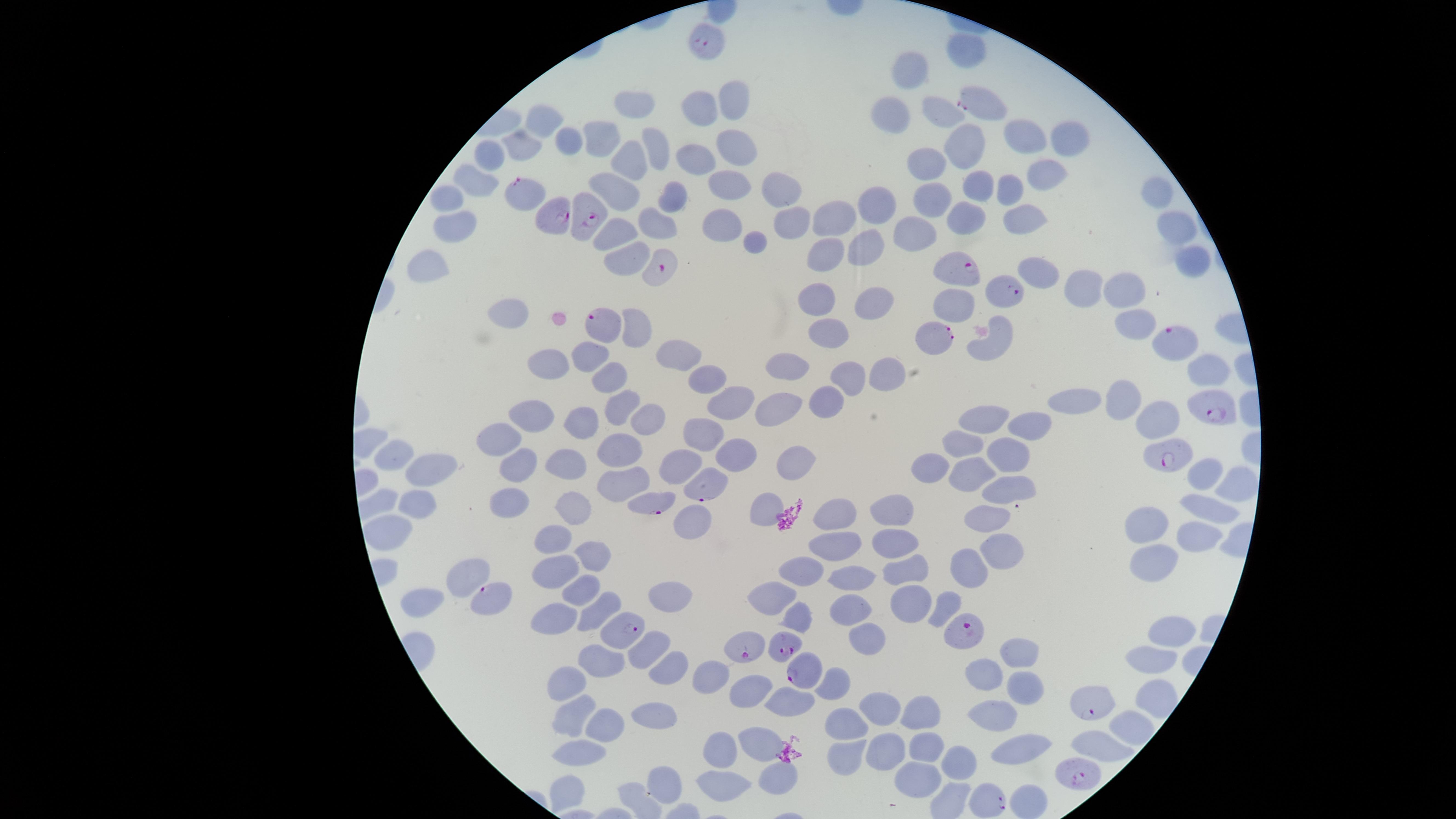
Approximate marker points as {x, y} in pixels. Uninfected RBCs: {966, 45}, {912, 68}, {733, 96}, {635, 103}, {700, 103}, {935, 107}, {894, 112}, {544, 116}, {1023, 134}, {1071, 139}, {608, 140}, {572, 143}, {528, 144}, {657, 145}, {732, 145}, {965, 145}, {491, 155}, {630, 158}, {692, 159}, {927, 165}, {1044, 169}, {728, 179}, {477, 181}, {981, 185}, {1160, 187}, {619, 188}, {780, 188}, {1011, 190}, {935, 193}, {449, 196}, {674, 198}, {877, 203}, {1022, 214}, {964, 216}, {834, 217}, {794, 220}, {723, 224}, {654, 225}, {455, 226}, {914, 227}, {1176, 227}, {617, 229}, {755, 240}, {862, 245}, {825, 253}, {630, 261}, {1189, 262}, {426, 264}, {1037, 270}, {1072, 284}, {1121, 286}, {870, 297}, {820, 298}, {950, 298}, {503, 313}, {1137, 322}, {637, 332}, {829, 332}, {991, 341}, {675, 351}, {588, 355}, {553, 365}, {1208, 366}, {889, 373}, {604, 375}, {793, 375}, {710, 381}, {852, 381}, {1121, 399}, {1078, 402}, {620, 403}, {831, 403}, {732, 405}, {782, 409}, {991, 409}, {648, 411}, {588, 415}, {536, 416}, {1154, 419}, {1028, 421}, {699, 429}, {499, 437}, {965, 441}, {1004, 446}, {737, 452}, {614, 454}, {398, 456}, {681, 459}, {788, 461}, {932, 464}, {514, 468}, {567, 468}, {432, 470}, {1205, 471}, {974, 472}, {627, 479}, {1232, 485}, {1011, 486}, {511, 501}, {901, 504}, {414, 505}, {573, 506}, {761, 508}, {1204, 508}, {992, 513}, {834, 516}, {690, 520}, {1148, 522}, {389, 528}, {555, 532}, {1193, 536}, {829, 538}, {889, 540}, {595, 545}, {1002, 554}, {1155, 561}, {554, 564}, {801, 570}, {903, 572}, {968, 572}, {464, 577}, {855, 579}, {583, 584}, {667, 593}, {769, 593}, {418, 597}, {913, 597}, {948, 603}, {557, 613}, {590, 613}, {794, 613}, {846, 613}, {1169, 629}, {863, 645}, {1016, 647}, {649, 649}, {1154, 654}, {603, 655}, {668, 669}, {704, 674}, {987, 674}, {560, 679}, {1023, 680}, {837, 682}, {745, 693}, {789, 698}, {575, 708}, {881, 708}, {920, 712}, {995, 715}, {655, 716}, {603, 719}, {1125, 724}, {845, 726}, {760, 735}, {1098, 744}, {927, 747}, {887, 750}, {719, 751}, {1019, 752}, {577, 754}, {848, 758}, {958, 760}, {777, 774}, {664, 778}, {569, 779}, {915, 780}, {720, 782}. Parasitized RBCs: {706, 43}, {983, 104}, {529, 193}, {554, 218}, {592, 218}, {662, 267}, {954, 269}, {1001, 294}, {603, 322}, {932, 337}, {1170, 338}, {1214, 409}, {1161, 456}, {703, 483}, {654, 503}, {489, 599}, {622, 632}, {970, 633}, {783, 644}, {744, 645}, {801, 674}, {1083, 704}, {1081, 779}, {987, 800}. Giemsa stain. Species: Plasmodium falciparum. Presence: malaria parasites seen. Smartphone photograph through the microscope eyepiece. Image is 1456×819 pixels. Thin smear of blood. Single field of view. The visible region is circular.